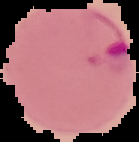

image type = segmented cell region on a black background
preparation = thin blood film
malaria status = parasitized
image size = 139×142 pixels